Outline each blood parasite and name the species.
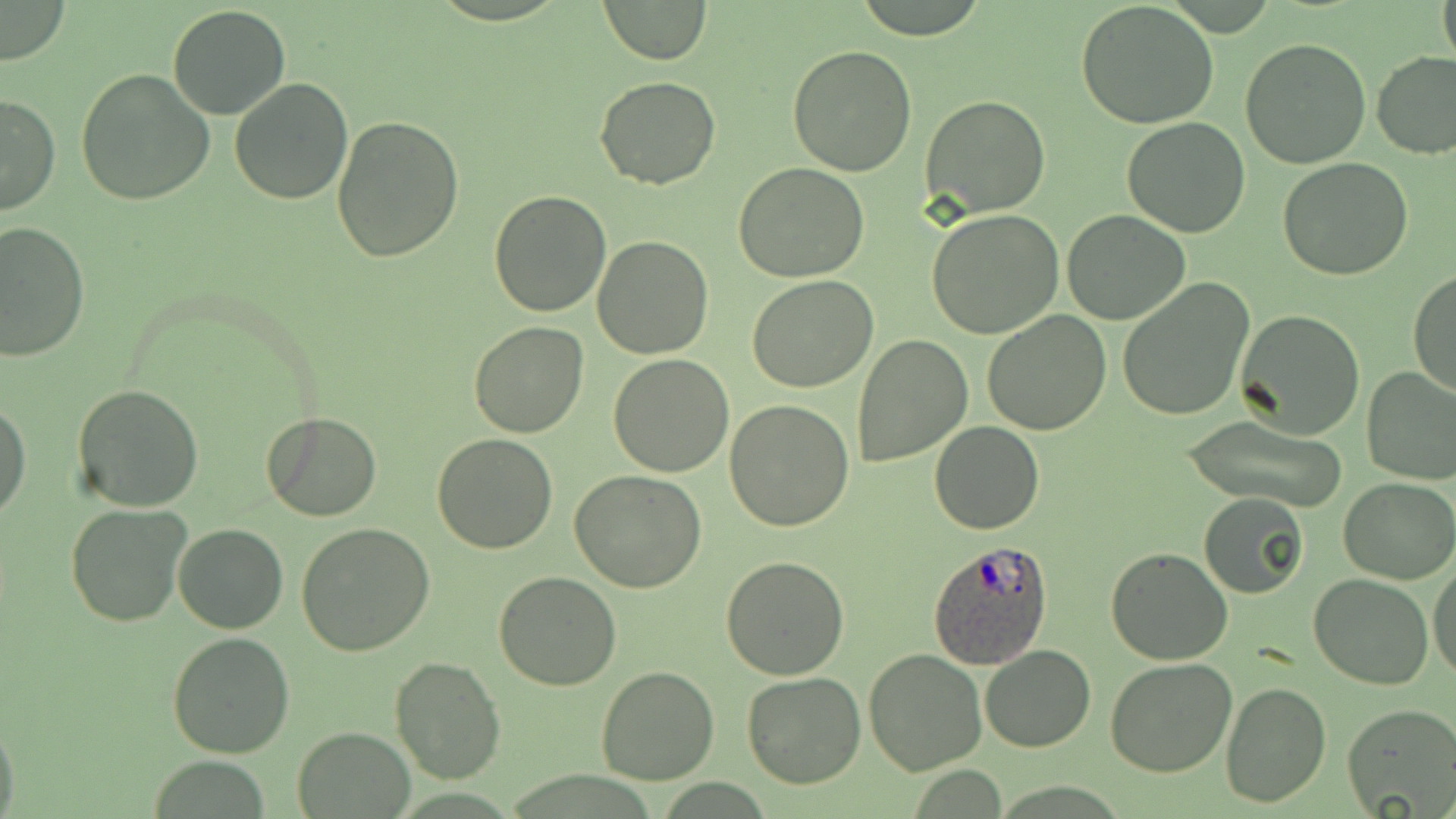

Approximate bounding boxes as [x1, y1, x2, y2] in pixels.
Plasmodium ovale-infected red blood cells: [928, 541, 1052, 669].
No Plasmodium falciparum, Plasmodium malariae, Plasmodium vivax, Babesia divergens, or Trypanosoma brucei observed.

Uninfected red blood cell locations: [599, 0, 711, 64], [1437, 0, 1456, 71], [1075, 1, 1218, 128], [0, 2, 70, 65], [168, 4, 291, 119], [1240, 38, 1371, 170], [787, 45, 916, 175], [1371, 51, 1456, 160], [76, 69, 215, 206], [593, 76, 721, 190], [228, 77, 354, 204], [0, 92, 60, 215], [921, 94, 1051, 218], [330, 115, 463, 262], [1122, 116, 1252, 237], [1278, 159, 1412, 281], [734, 163, 869, 282], [489, 190, 612, 317], [926, 208, 1063, 337], [1062, 210, 1191, 326], [0, 221, 90, 362], [590, 236, 713, 359], [1408, 268, 1456, 399], [748, 273, 878, 392], [1116, 278, 1255, 421], [981, 309, 1112, 435], [1234, 309, 1365, 439], [469, 322, 591, 439], [851, 334, 972, 468], [608, 354, 733, 477], [1361, 365, 1456, 486], [72, 384, 204, 514], [0, 398, 30, 523], [725, 401, 855, 534], [261, 412, 383, 521], [1181, 415, 1351, 514], [930, 420, 1045, 534], [432, 433, 560, 553], [571, 470, 706, 591], [1339, 477, 1455, 585], [1198, 491, 1309, 598], [66, 503, 193, 628], [296, 522, 435, 656], [173, 524, 288, 633], [1105, 547, 1233, 665], [721, 556, 851, 679], [1429, 558, 1456, 682], [493, 571, 623, 692], [1308, 574, 1434, 690], [167, 631, 294, 758], [979, 645, 1096, 754], [862, 648, 987, 775], [1105, 655, 1238, 776], [389, 657, 504, 787], [595, 666, 720, 785], [740, 673, 868, 789], [1221, 680, 1332, 808], [1341, 703, 1456, 818], [0, 715, 21, 819], [293, 728, 414, 817]. Slide-level diagnosis: Plasmodium ovale. Captured at 1000x magnification. Image is 1456×819 pixels. May-Grünwald-Giemsa stain. One field of a larger specimen. Optical microscopy. Thin blood smear.